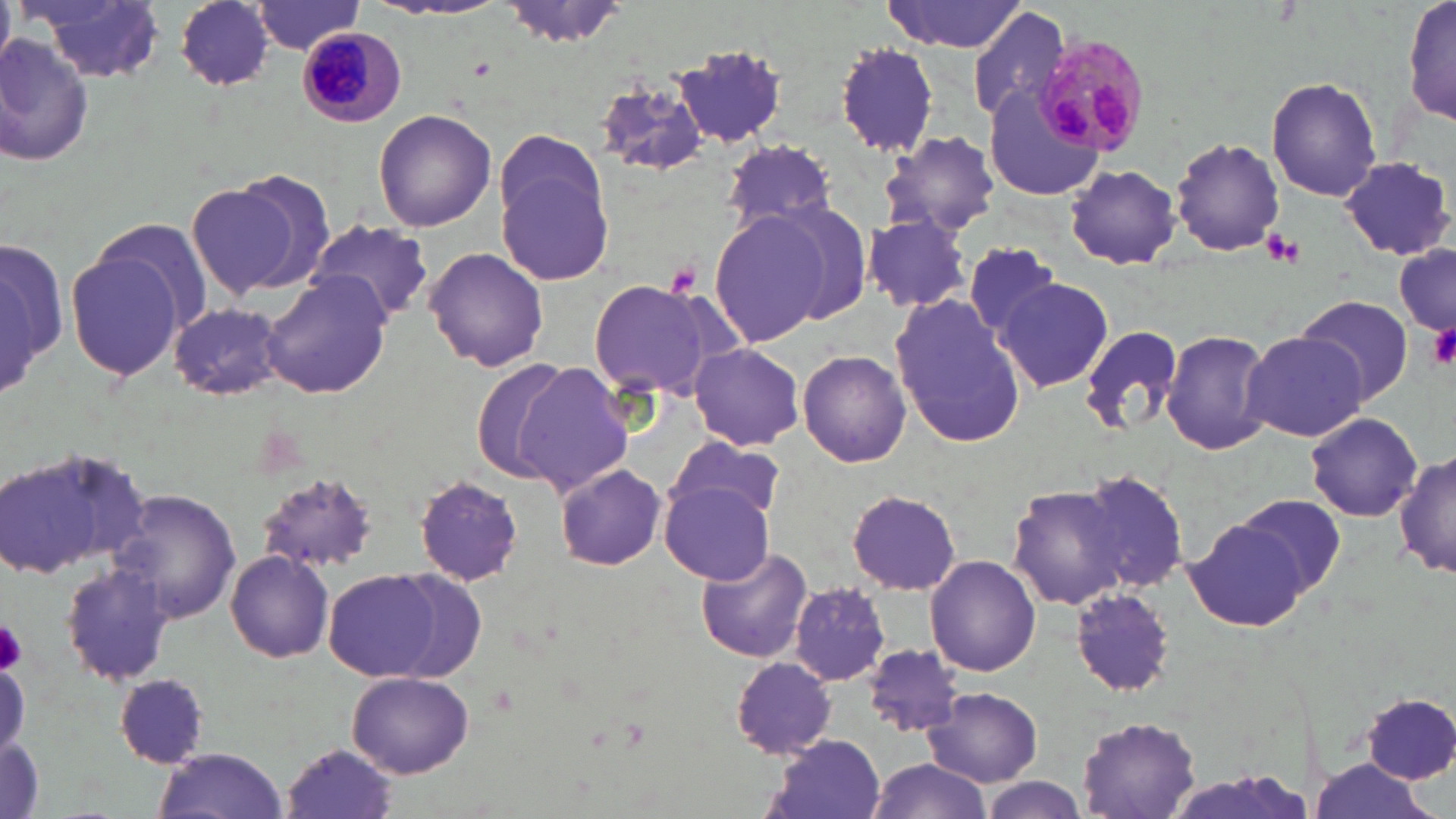

{
  "slide_level_diagnosis": "Plasmodium malariae",
  "image_size": "1456×819 pixels",
  "uninfected_red_blood_cell_locations": "approximate bounding boxes as named x1/y1/x2/y2 corners in pixels: (x1=0, y1=0, x2=14, y2=66), (x1=174, y1=0, x2=278, y2=90), (x1=498, y1=0, x2=630, y2=47), (x1=883, y1=0, x2=1032, y2=53), (x1=1403, y1=0, x2=1454, y2=132), (x1=34, y1=1, x2=168, y2=85), (x1=249, y1=2, x2=367, y2=56), (x1=968, y1=6, x2=1071, y2=123), (x1=1, y1=31, x2=98, y2=171), (x1=834, y1=41, x2=942, y2=158), (x1=675, y1=48, x2=790, y2=149), (x1=593, y1=75, x2=712, y2=180), (x1=1265, y1=76, x2=1384, y2=203), (x1=985, y1=90, x2=1103, y2=200), (x1=373, y1=107, x2=497, y2=232), (x1=879, y1=131, x2=1000, y2=237), (x1=492, y1=133, x2=617, y2=287), (x1=1171, y1=137, x2=1285, y2=257), (x1=719, y1=139, x2=840, y2=237), (x1=1339, y1=155, x2=1453, y2=260), (x1=1065, y1=164, x2=1182, y2=270), (x1=193, y1=171, x2=333, y2=299), (x1=768, y1=199, x2=874, y2=324), (x1=709, y1=211, x2=832, y2=347), (x1=861, y1=214, x2=975, y2=316), (x1=306, y1=220, x2=436, y2=326), (x1=92, y1=221, x2=214, y2=335), (x1=1, y1=237, x2=66, y2=401), (x1=1393, y1=239, x2=1455, y2=342), (x1=963, y1=240, x2=1063, y2=342), (x1=63, y1=247, x2=190, y2=386), (x1=423, y1=247, x2=549, y2=373), (x1=259, y1=271, x2=392, y2=400), (x1=994, y1=274, x2=1114, y2=393), (x1=588, y1=279, x2=717, y2=397), (x1=1293, y1=294, x2=1416, y2=407), (x1=890, y1=295, x2=1025, y2=450), (x1=166, y1=301, x2=292, y2=402), (x1=1076, y1=323, x2=1185, y2=436), (x1=1161, y1=329, x2=1274, y2=457), (x1=1240, y1=330, x2=1368, y2=444), (x1=687, y1=342, x2=806, y2=451), (x1=798, y1=350, x2=911, y2=468), (x1=469, y1=360, x2=572, y2=486), (x1=515, y1=364, x2=636, y2=497), (x1=1305, y1=413, x2=1423, y2=522), (x1=664, y1=436, x2=784, y2=529), (x1=0, y1=448, x2=150, y2=582), (x1=1393, y1=451, x2=1455, y2=580), (x1=554, y1=463, x2=666, y2=571), (x1=1077, y1=467, x2=1192, y2=596), (x1=254, y1=472, x2=380, y2=577), (x1=414, y1=473, x2=524, y2=587), (x1=662, y1=481, x2=775, y2=584), (x1=1008, y1=484, x2=1131, y2=611), (x1=847, y1=488, x2=961, y2=596), (x1=111, y1=490, x2=241, y2=624), (x1=1235, y1=494, x2=1348, y2=598), (x1=1183, y1=519, x2=1314, y2=634), (x1=695, y1=546, x2=813, y2=663), (x1=225, y1=550, x2=333, y2=663), (x1=926, y1=554, x2=1043, y2=677), (x1=59, y1=563, x2=180, y2=687), (x1=324, y1=570, x2=449, y2=681), (x1=389, y1=571, x2=487, y2=681), (x1=791, y1=583, x2=892, y2=686), (x1=1067, y1=586, x2=1174, y2=696), (x1=860, y1=644, x2=963, y2=736), (x1=731, y1=657, x2=839, y2=760), (x1=348, y1=672, x2=473, y2=778), (x1=117, y1=675, x2=209, y2=767), (x1=923, y1=689, x2=1045, y2=784), (x1=1360, y1=693, x2=1453, y2=784), (x1=1076, y1=717, x2=1203, y2=817), (x1=0, y1=733, x2=45, y2=819), (x1=763, y1=736, x2=887, y2=819), (x1=278, y1=740, x2=399, y2=819), (x1=150, y1=750, x2=292, y2=819), (x1=1303, y1=760, x2=1438, y2=819), (x1=861, y1=761, x2=995, y2=819), (x1=977, y1=778, x2=1092, y2=819)",
  "field_of_view": "single",
  "preparation": "thin blood film",
  "platelet_locations": "approximate bounding boxes as named x1/y1/x2/y2 corners in pixels: (x1=1262, y1=230, x2=1304, y2=269), (x1=664, y1=260, x2=700, y2=297), (x1=1427, y1=323, x2=1456, y2=368), (x1=0, y1=618, x2=27, y2=675)",
  "stain": "May-Grünwald-Giemsa",
  "magnification": "1000x",
  "plasmodium_malariae_infected_red_blood_cell_locations": "approximate bounding boxes as named x1/y1/x2/y2 corners in pixels: (x1=296, y1=26, x2=407, y2=129), (x1=1027, y1=32, x2=1147, y2=157)",
  "modality": "light microscopy"
}